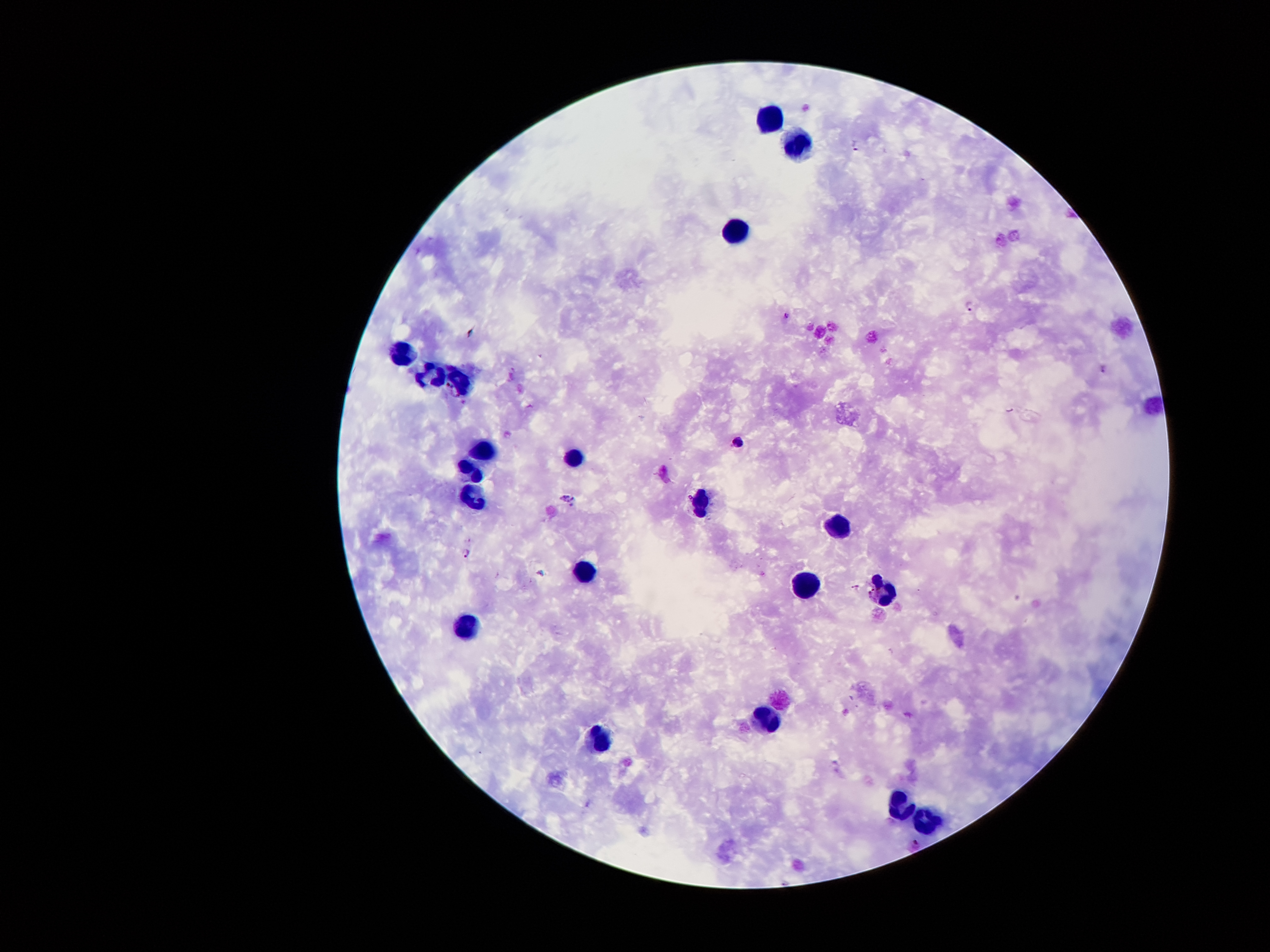
Approximate centers as {x, y} in pixels. Leukocyte locations: {768, 118}, {798, 145}, {736, 238}, {401, 351}, {428, 376}, {460, 379}, {489, 452}, {575, 453}, {468, 470}, {475, 498}, {700, 501}, {840, 532}, {585, 571}, {807, 585}, {883, 595}, {466, 625}, {771, 721}, {602, 741}, {899, 806}, {926, 820}. Plasmodium parasite locations: {856, 145}, {970, 308}, {786, 316}, {1102, 367}, {739, 441}, {567, 499}, {467, 553}, {542, 573}, {856, 587}. 100x magnification. Single field of view. Thick peripheral-blood smear. Image is 1270×952 pixels. Patient malaria status: positive for Plasmodium falciparum. Smartphone photograph taken through the microscope eyepiece. Giemsa stain.